Outline each Plasmodium falciparum-infected red blood cell.
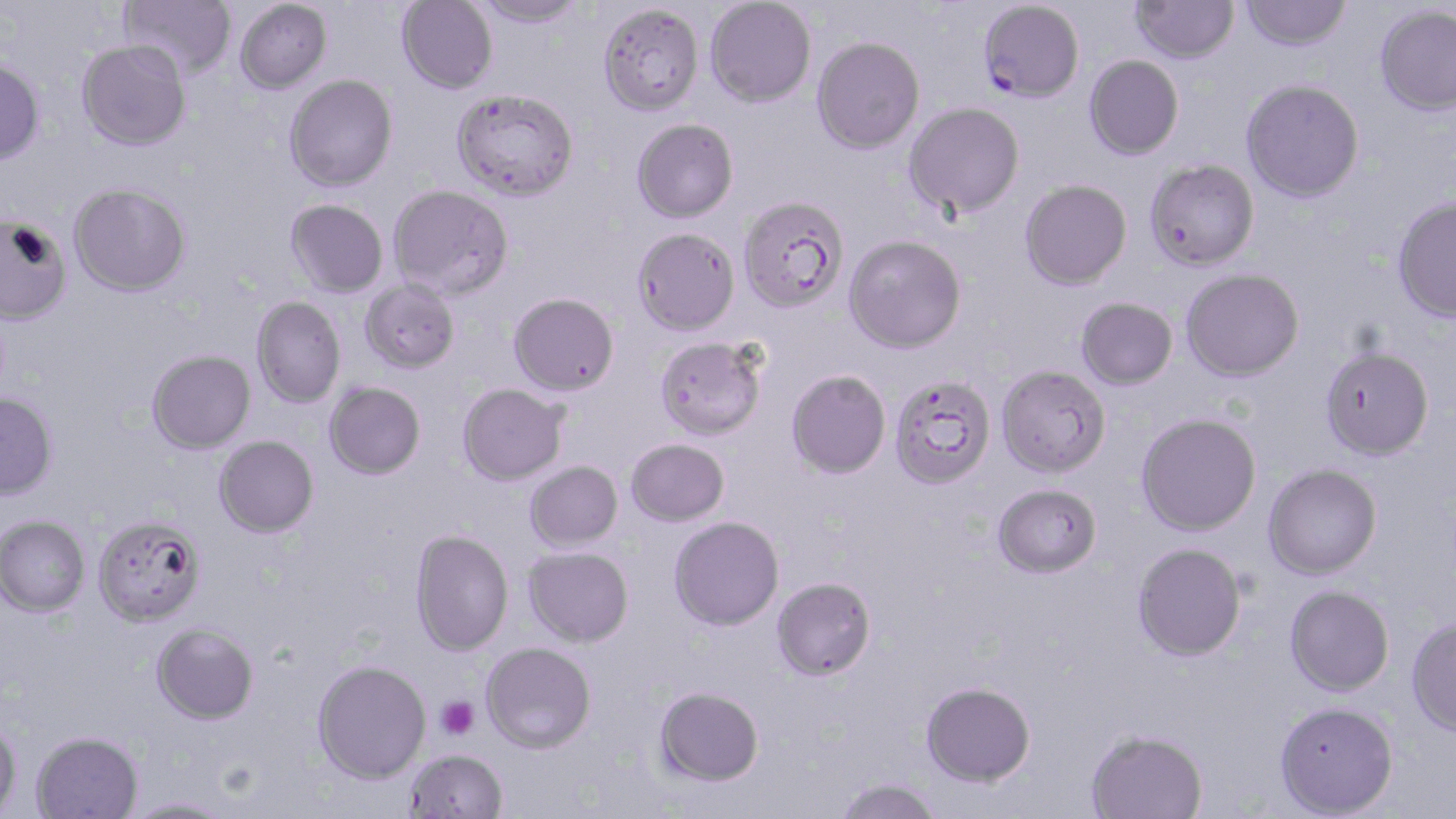

Approximate bounding boxes as named x1/y1/x2/y2 corners in pixels.
Plasmodium falciparum-infected red blood cells: (x1=978, y1=0, x2=1085, y2=102).

Uninfected red blood cell locations: (x1=120, y1=0, x2=236, y2=80), (x1=234, y1=0, x2=333, y2=94), (x1=396, y1=0, x2=498, y2=93), (x1=470, y1=0, x2=587, y2=28), (x1=705, y1=1, x2=816, y2=107), (x1=1131, y1=1, x2=1240, y2=63), (x1=1240, y1=1, x2=1352, y2=51), (x1=598, y1=3, x2=705, y2=115), (x1=1375, y1=4, x2=1456, y2=116), (x1=812, y1=36, x2=925, y2=154), (x1=77, y1=40, x2=192, y2=151), (x1=1084, y1=55, x2=1184, y2=159), (x1=0, y1=58, x2=45, y2=166), (x1=284, y1=74, x2=398, y2=192), (x1=1241, y1=78, x2=1365, y2=202), (x1=452, y1=88, x2=579, y2=202), (x1=904, y1=102, x2=1025, y2=218), (x1=631, y1=117, x2=739, y2=223), (x1=1144, y1=159, x2=1259, y2=270), (x1=1019, y1=179, x2=1132, y2=290), (x1=69, y1=183, x2=191, y2=296), (x1=388, y1=184, x2=514, y2=299), (x1=738, y1=195, x2=849, y2=314), (x1=1391, y1=197, x2=1456, y2=321), (x1=285, y1=199, x2=388, y2=298), (x1=1, y1=216, x2=72, y2=326), (x1=632, y1=227, x2=740, y2=337), (x1=844, y1=235, x2=966, y2=353), (x1=1181, y1=268, x2=1304, y2=381), (x1=359, y1=279, x2=461, y2=374), (x1=508, y1=292, x2=619, y2=396), (x1=251, y1=296, x2=346, y2=408), (x1=1076, y1=297, x2=1178, y2=390), (x1=655, y1=337, x2=766, y2=441), (x1=1319, y1=345, x2=1434, y2=460), (x1=147, y1=349, x2=256, y2=454), (x1=996, y1=365, x2=1110, y2=478), (x1=786, y1=370, x2=891, y2=479), (x1=888, y1=375, x2=997, y2=490), (x1=324, y1=382, x2=426, y2=480), (x1=457, y1=384, x2=568, y2=485), (x1=0, y1=394, x2=58, y2=501), (x1=1136, y1=412, x2=1262, y2=536), (x1=214, y1=435, x2=319, y2=538), (x1=626, y1=438, x2=729, y2=526), (x1=524, y1=461, x2=623, y2=552), (x1=1262, y1=464, x2=1382, y2=580), (x1=993, y1=483, x2=1103, y2=579), (x1=0, y1=515, x2=90, y2=617), (x1=93, y1=516, x2=206, y2=628), (x1=668, y1=516, x2=785, y2=631), (x1=410, y1=529, x2=514, y2=656), (x1=1132, y1=542, x2=1246, y2=661), (x1=524, y1=546, x2=634, y2=647), (x1=772, y1=576, x2=877, y2=680), (x1=1284, y1=585, x2=1394, y2=697), (x1=1406, y1=617, x2=1456, y2=736), (x1=152, y1=623, x2=258, y2=725), (x1=481, y1=641, x2=596, y2=753), (x1=311, y1=659, x2=431, y2=783), (x1=921, y1=681, x2=1035, y2=786), (x1=654, y1=686, x2=764, y2=786), (x1=1274, y1=701, x2=1398, y2=817), (x1=0, y1=716, x2=22, y2=817), (x1=1085, y1=728, x2=1208, y2=819), (x1=31, y1=731, x2=143, y2=818), (x1=405, y1=749, x2=508, y2=819), (x1=835, y1=777, x2=942, y2=819), (x1=119, y1=797, x2=233, y2=818). Platelet locations: (x1=435, y1=696, x2=480, y2=739). Slide-level diagnosis: Plasmodium falciparum. One field of a larger specimen. Thin blood film. Captured at 1000x magnification. Optical microscopy. Image is 1456×819 pixels. May-Grünwald-Giemsa stain.